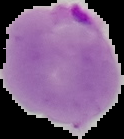
Summary:
  - Preparation: thin blood smear
  - Malaria status: parasitized
  - Image size: 124×139 pixels
  - Image type: segmented cell region with the area outside set to black